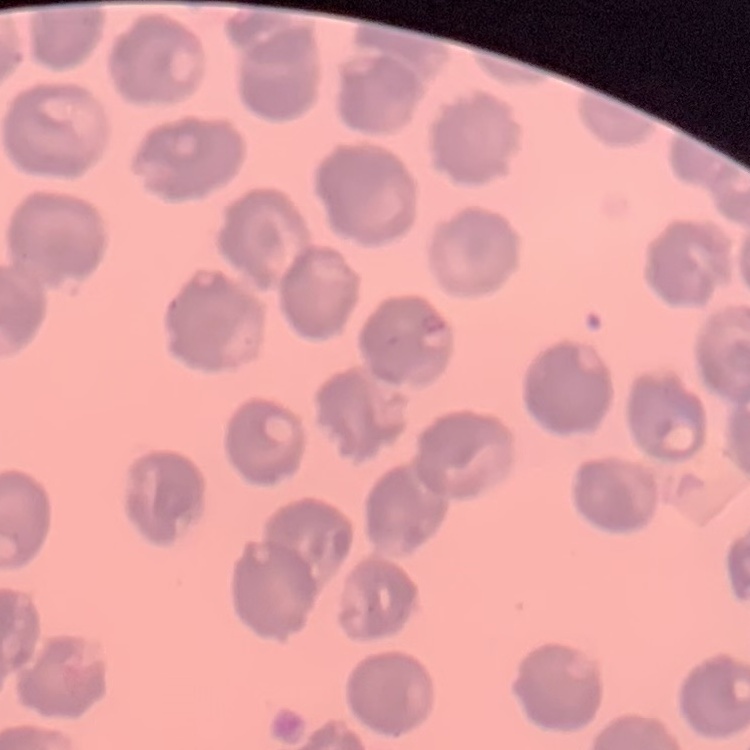
The red blood cells show no rouleaux formation. One tile cut from a larger photomicrograph. Field's or Giemsa stain. Thin blood smear.